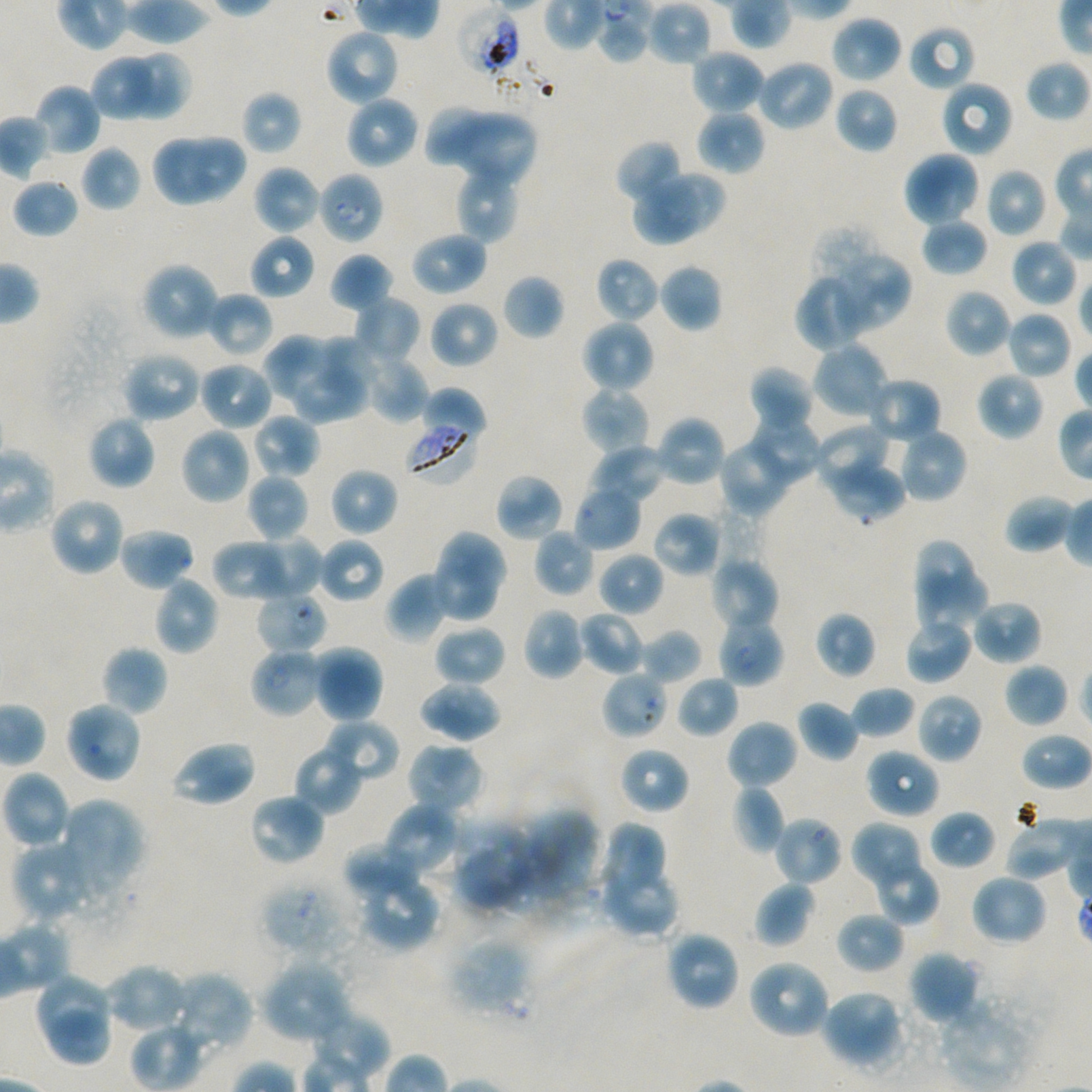 Approximate bounding rectangles given as corner coordinates in pixels from the top-left. Not every red blood cell is marked. A life-cycle stage — or a range of stages, where the recorded stages span more than one — follows each staged infected red blood cell. Locations of infected red blood cells: (x1=405, y1=416, x2=480, y2=484); (x1=255, y1=590, x2=327, y2=655) early ring; (x1=717, y1=615, x2=785, y2=687) ring. Locations of uninfected red blood cells: (x1=831, y1=15, x2=903, y2=84), (x1=908, y1=24, x2=976, y2=92), (x1=325, y1=29, x2=401, y2=107), (x1=690, y1=49, x2=765, y2=116), (x1=126, y1=50, x2=191, y2=118), (x1=91, y1=54, x2=153, y2=121), (x1=754, y1=59, x2=835, y2=131), (x1=1025, y1=59, x2=1089, y2=122), (x1=939, y1=79, x2=1014, y2=158), (x1=33, y1=84, x2=101, y2=157), (x1=834, y1=86, x2=898, y2=153), (x1=241, y1=90, x2=302, y2=156), (x1=345, y1=96, x2=420, y2=170), (x1=423, y1=103, x2=487, y2=166), (x1=697, y1=109, x2=765, y2=175), (x1=451, y1=114, x2=537, y2=187), (x1=151, y1=132, x2=219, y2=206), (x1=188, y1=134, x2=244, y2=198), (x1=615, y1=139, x2=683, y2=204), (x1=81, y1=145, x2=141, y2=212), (x1=903, y1=150, x2=981, y2=228), (x1=253, y1=164, x2=321, y2=236), (x1=455, y1=164, x2=522, y2=243), (x1=985, y1=166, x2=1049, y2=238), (x1=663, y1=170, x2=727, y2=227), (x1=12, y1=179, x2=79, y2=238), (x1=631, y1=183, x2=706, y2=246), (x1=921, y1=217, x2=988, y2=277), (x1=410, y1=230, x2=489, y2=296), (x1=249, y1=234, x2=315, y2=300), (x1=1010, y1=238, x2=1077, y2=308), (x1=830, y1=251, x2=912, y2=332), (x1=329, y1=252, x2=395, y2=313), (x1=595, y1=257, x2=661, y2=324), (x1=141, y1=261, x2=220, y2=342), (x1=659, y1=263, x2=723, y2=333), (x1=793, y1=272, x2=872, y2=352), (x1=502, y1=274, x2=564, y2=340), (x1=945, y1=289, x2=1011, y2=357), (x1=206, y1=291, x2=274, y2=359), (x1=353, y1=295, x2=420, y2=363), (x1=429, y1=300, x2=499, y2=369), (x1=1006, y1=310, x2=1072, y2=380), (x1=580, y1=318, x2=655, y2=393), (x1=314, y1=333, x2=380, y2=393), (x1=265, y1=334, x2=337, y2=405), (x1=812, y1=342, x2=890, y2=420), (x1=122, y1=350, x2=202, y2=423), (x1=361, y1=352, x2=429, y2=423), (x1=197, y1=360, x2=274, y2=431), (x1=748, y1=365, x2=814, y2=437), (x1=291, y1=367, x2=371, y2=422), (x1=976, y1=371, x2=1045, y2=441), (x1=866, y1=376, x2=942, y2=444), (x1=420, y1=386, x2=487, y2=444), (x1=580, y1=387, x2=652, y2=456), (x1=252, y1=413, x2=320, y2=479), (x1=88, y1=414, x2=157, y2=490), (x1=654, y1=414, x2=727, y2=488), (x1=747, y1=418, x2=821, y2=484), (x1=812, y1=424, x2=892, y2=492), (x1=179, y1=426, x2=254, y2=505), (x1=896, y1=426, x2=968, y2=504), (x1=718, y1=439, x2=789, y2=516), (x1=589, y1=444, x2=668, y2=505), (x1=827, y1=454, x2=907, y2=523), (x1=329, y1=467, x2=399, y2=536), (x1=246, y1=473, x2=310, y2=541), (x1=494, y1=473, x2=564, y2=542), (x1=574, y1=484, x2=642, y2=551), (x1=1004, y1=494, x2=1074, y2=553), (x1=48, y1=496, x2=126, y2=577), (x1=653, y1=511, x2=723, y2=577), (x1=117, y1=526, x2=194, y2=592), (x1=533, y1=528, x2=596, y2=597), (x1=437, y1=531, x2=511, y2=600), (x1=249, y1=535, x2=323, y2=602), (x1=317, y1=537, x2=384, y2=603), (x1=211, y1=539, x2=290, y2=601), (x1=912, y1=539, x2=975, y2=602), (x1=597, y1=551, x2=663, y2=617), (x1=710, y1=556, x2=780, y2=633), (x1=428, y1=558, x2=500, y2=623), (x1=386, y1=572, x2=450, y2=642), (x1=916, y1=572, x2=989, y2=633), (x1=153, y1=575, x2=220, y2=655), (x1=971, y1=600, x2=1042, y2=666), (x1=522, y1=607, x2=587, y2=681), (x1=579, y1=611, x2=646, y2=676), (x1=815, y1=611, x2=876, y2=679), (x1=904, y1=617, x2=972, y2=685), (x1=434, y1=624, x2=507, y2=688), (x1=640, y1=628, x2=702, y2=685), (x1=101, y1=645, x2=168, y2=717), (x1=312, y1=645, x2=384, y2=723), (x1=1004, y1=663, x2=1069, y2=728), (x1=676, y1=675, x2=739, y2=738), (x1=418, y1=680, x2=502, y2=742), (x1=851, y1=685, x2=915, y2=738), (x1=915, y1=692, x2=984, y2=763), (x1=797, y1=699, x2=860, y2=762), (x1=63, y1=700, x2=143, y2=784), (x1=321, y1=718, x2=400, y2=782), (x1=725, y1=718, x2=799, y2=790), (x1=169, y1=740, x2=257, y2=807), (x1=405, y1=742, x2=486, y2=818), (x1=293, y1=746, x2=362, y2=816), (x1=619, y1=746, x2=690, y2=815), (x1=864, y1=748, x2=940, y2=819), (x1=2, y1=770, x2=71, y2=850), (x1=731, y1=784, x2=786, y2=854), (x1=248, y1=793, x2=326, y2=867), (x1=59, y1=798, x2=146, y2=894), (x1=382, y1=802, x2=463, y2=879), (x1=517, y1=809, x2=602, y2=909), (x1=930, y1=809, x2=996, y2=870), (x1=773, y1=816, x2=843, y2=886), (x1=1004, y1=818, x2=1085, y2=877), (x1=452, y1=819, x2=537, y2=913), (x1=851, y1=820, x2=926, y2=888), (x1=596, y1=822, x2=671, y2=911), (x1=12, y1=840, x2=98, y2=924), (x1=342, y1=843, x2=424, y2=901), (x1=875, y1=864, x2=939, y2=926), (x1=601, y1=873, x2=681, y2=937), (x1=969, y1=873, x2=1048, y2=947), (x1=357, y1=875, x2=439, y2=951), (x1=754, y1=881, x2=814, y2=947), (x1=835, y1=911, x2=905, y2=974), (x1=665, y1=929, x2=741, y2=1011), (x1=449, y1=937, x2=532, y2=1017), (x1=907, y1=949, x2=981, y2=1025), (x1=746, y1=958, x2=831, y2=1040), (x1=260, y1=960, x2=352, y2=1044), (x1=103, y1=963, x2=188, y2=1034), (x1=168, y1=970, x2=253, y2=1055), (x1=33, y1=972, x2=110, y2=1041), (x1=820, y1=989, x2=903, y2=1070), (x1=933, y1=996, x2=1037, y2=1089), (x1=47, y1=1011, x2=109, y2=1066). Locations of red blood cells of indeterminate infection status: (x1=457, y1=5, x2=522, y2=79), (x1=596, y1=5, x2=649, y2=64), (x1=317, y1=171, x2=384, y2=245), (x1=249, y1=647, x2=325, y2=718), (x1=601, y1=670, x2=669, y2=740), (x1=261, y1=877, x2=357, y2=960). 100x oil-immersion objective, numerical aperture 1.45. Giemsa stain. Thin blood smear. Image is 1092×1092 pixels. Single field of view. Donor blood group A+/O+. Plasmodium falciparum strain NF54 in static in-vitro culture.